Outline every leukocyte.
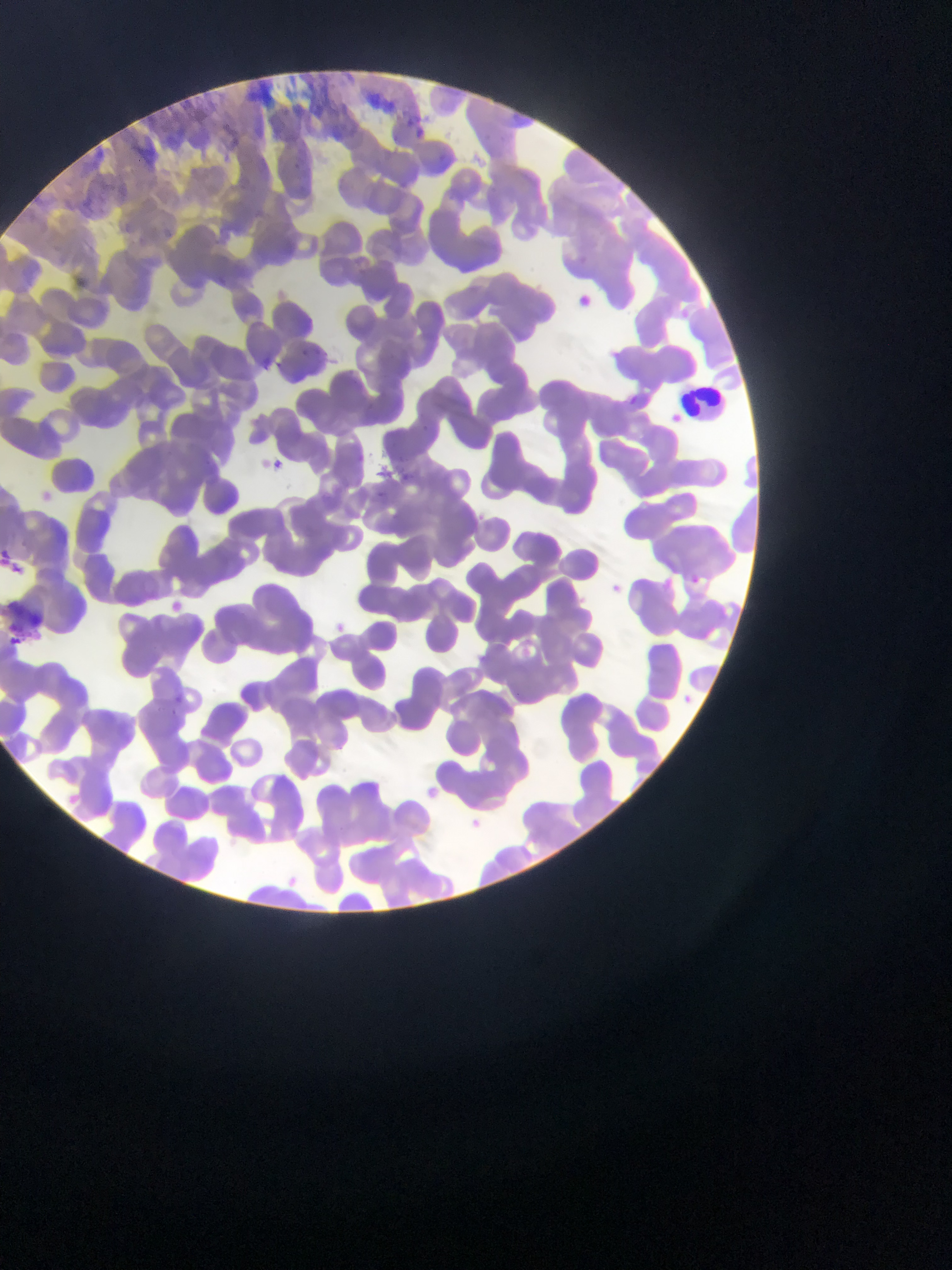

Approximate bounding boxes as left top right bottom in pixels.
Leukocytes: 679 389 725 420.

Summary:
  - Plasmodium parasite locations: 414 127 425 136; 302 349 313 357; 275 362 283 370; 629 395 637 403; 422 423 428 431; 261 455 289 478; 31 486 60 510; 685 571 705 588; 605 580 627 598; 160 597 188 620; 324 617 352 641; 10 634 21 645; 677 689 699 709; 175 694 183 704; 173 707 179 716; 462 813 488 835
  - Capture: mobile-phone photograph through a microscope
  - Image size: 952×1270 pixels
  - Field of view: single
  - Preparation: thin blood film
  - Country: Ghana